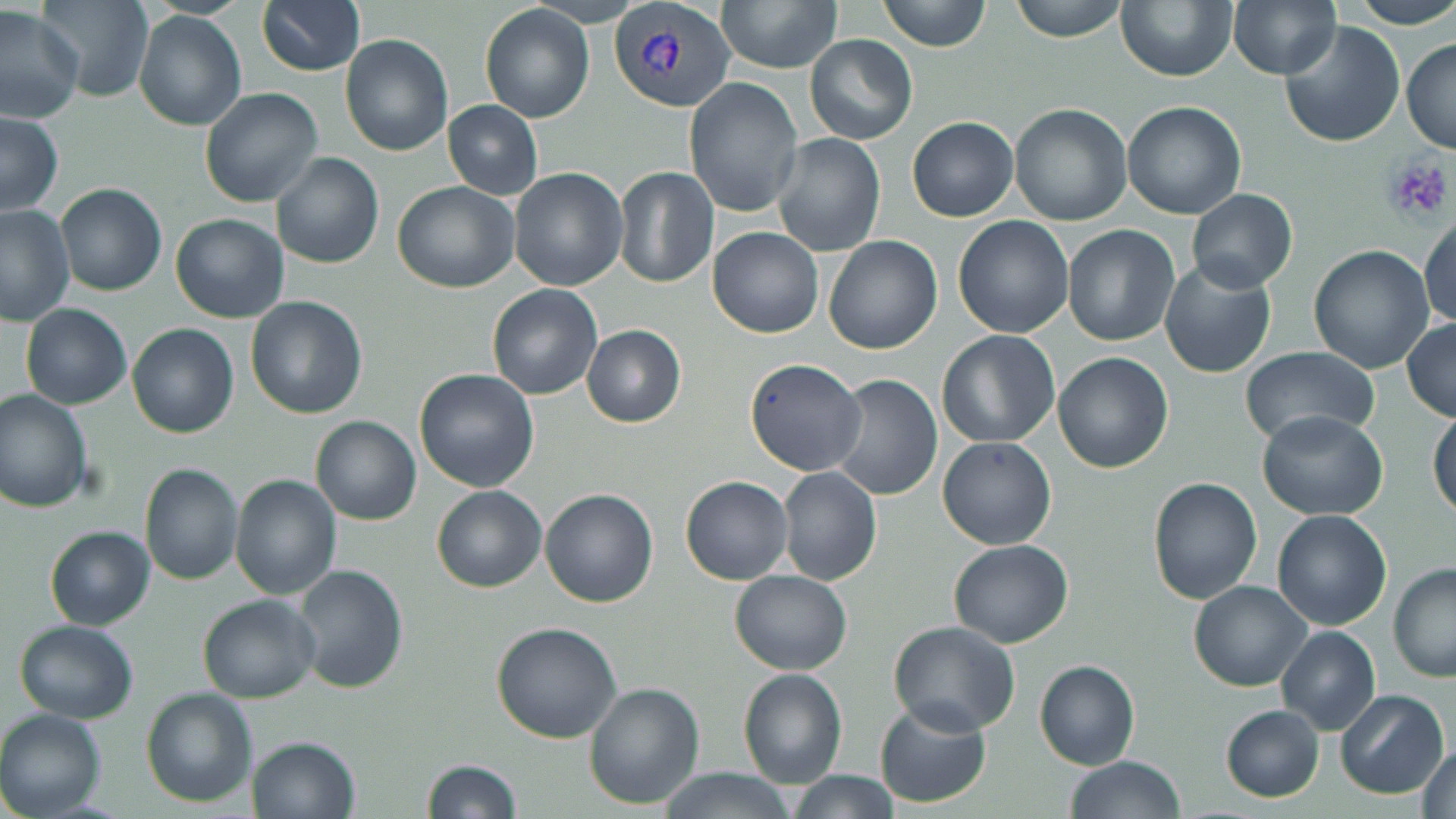 Approximate bounding boxes as (x1,y1)-(x2,y2) corner pairs in pixels. Plasmodium vivax-infected red blood cell locations: (609,2)-(736,113). Platelet locations: (1381,153)-(1455,227). Uninfected red blood cell locations: (257,0)-(365,75), (716,0)-(842,74), (875,0)-(994,52), (1008,0)-(1130,43), (1115,0)-(1237,82), (1347,0)-(1456,28), (38,1)-(154,102), (1228,2)-(1337,78), (480,4)-(594,123), (0,5)-(84,124), (134,11)-(245,131), (1277,20)-(1407,149), (339,33)-(453,157), (804,34)-(917,145), (1401,37)-(1455,155), (683,76)-(803,217), (199,87)-(323,207), (1121,100)-(1248,220), (442,101)-(542,199), (1008,102)-(1132,225), (1,110)-(64,216), (907,116)-(1019,222), (772,133)-(885,257), (271,152)-(384,270), (509,167)-(628,291), (613,167)-(717,288), (393,181)-(520,292), (56,184)-(167,297), (1187,188)-(1297,293), (0,205)-(73,328), (169,213)-(289,323), (1419,214)-(1456,329), (953,216)-(1075,337), (1062,225)-(1182,347), (708,226)-(823,339), (823,236)-(942,355), (1308,246)-(1438,374), (1159,261)-(1278,379), (486,283)-(603,400), (245,296)-(367,421), (20,304)-(132,410), (1402,318)-(1456,422), (129,324)-(240,438), (582,325)-(686,427), (937,329)-(1060,448), (1238,347)-(1379,450), (1053,352)-(1173,473), (743,358)-(868,476), (414,369)-(540,493), (828,374)-(942,502), (0,390)-(92,514), (1428,407)-(1456,524), (1257,410)-(1388,521), (311,416)-(422,525), (938,436)-(1056,549), (137,464)-(244,585), (777,467)-(881,585), (229,474)-(341,600), (680,476)-(793,585), (1148,476)-(1263,606), (432,485)-(547,593), (539,489)-(659,608), (1271,509)-(1392,631), (45,527)-(156,630), (948,540)-(1073,649), (1388,563)-(1456,683), (293,564)-(408,694), (730,569)-(852,676), (1188,580)-(1311,691), (197,594)-(322,703), (13,619)-(140,723), (889,620)-(1021,734), (491,621)-(623,743), (1276,625)-(1380,734), (1035,659)-(1141,770), (737,667)-(848,788), (584,682)-(704,809), (141,687)-(258,808), (1335,689)-(1449,799), (873,700)-(991,806), (1221,704)-(1324,802), (0,709)-(109,819), (246,735)-(361,819), (1415,743)-(1456,819), (1064,755)-(1187,819), (423,759)-(522,818), (655,768)-(802,819), (791,770)-(902,819). Slide-level diagnosis: Plasmodium vivax. Image is 1456×819 pixels. 1000x magnification. Thin blood film. May-Grünwald-Giemsa stain. One field of a larger specimen. Light microscopy.